Comment on the morphology of the red blood cells.
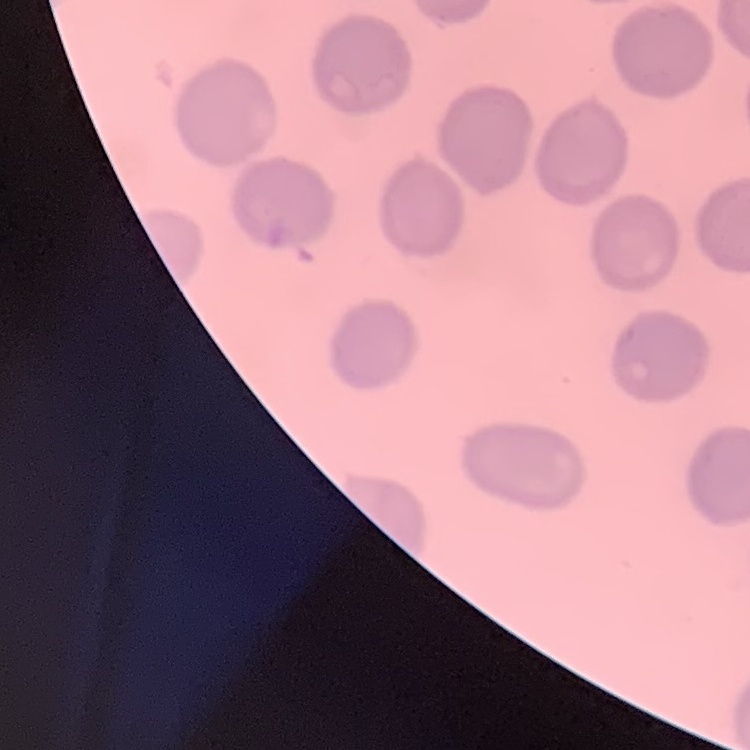
No rouleaux formation.

image type = one tile cut from a larger photomicrograph
preparation = thin blood film
stain = Field's or Giemsa